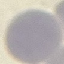
Summary:
  - Result: no malaria parasites seen
  - Image type: cell patch, automatically extracted from a larger field of view and resized to 64 × 64 pixels
  - Stain: Giemsa
  - Capture: smartphone through the microscope eyepiece
  - Preparation: thin blood film